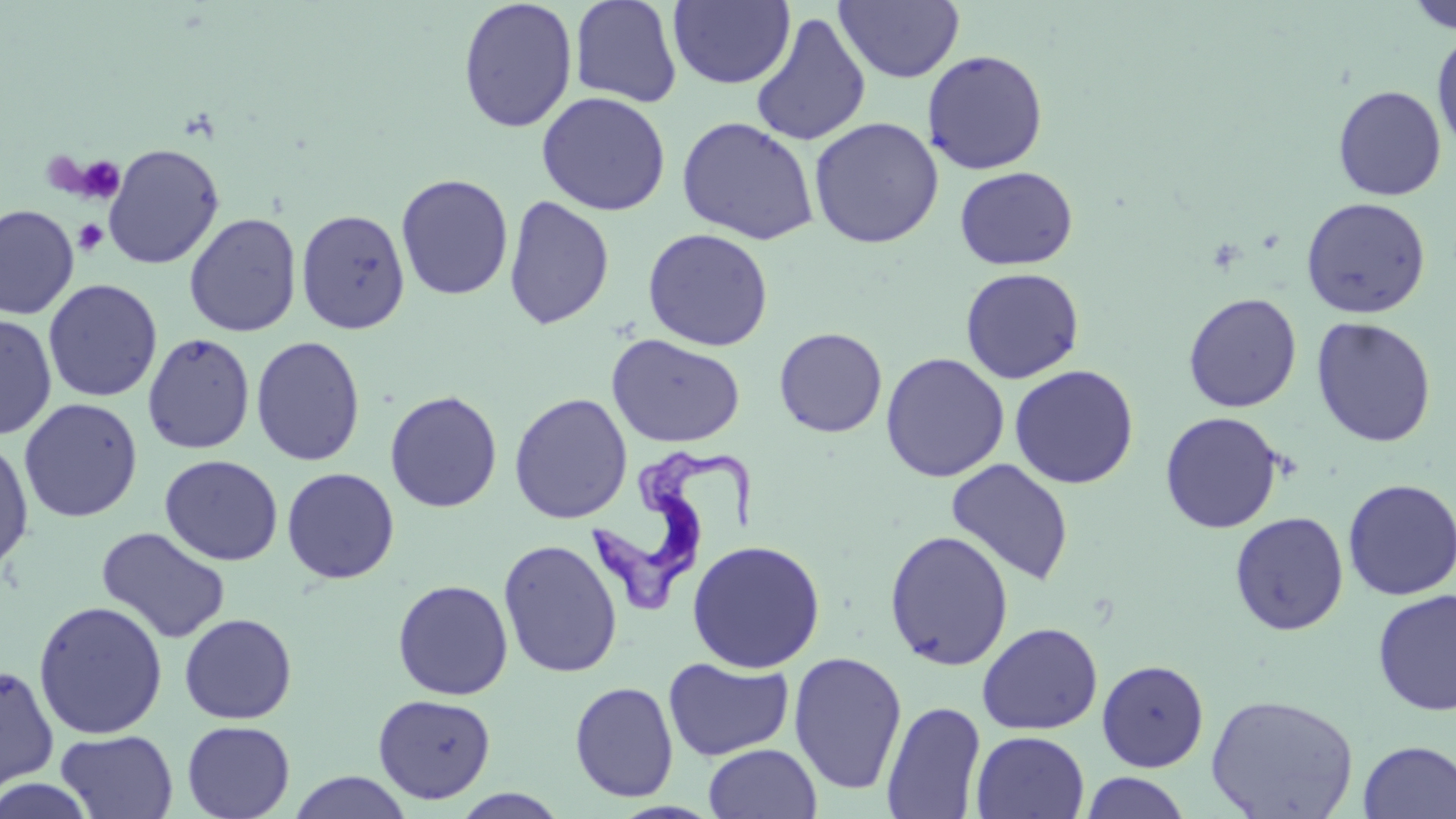

Approximate bounding boxes as (x1, y1, x2, y2) in pixels. Trypanosoma brucei locations: (582, 449, 760, 616). Uninfected red blood cell locations: (457, 0, 578, 133), (569, 0, 683, 109), (669, 0, 795, 89), (835, 1, 965, 84), (1406, 2, 1456, 34), (751, 12, 872, 147), (1432, 30, 1456, 158), (921, 49, 1048, 175), (1332, 85, 1447, 201), (536, 91, 670, 216), (676, 116, 820, 245), (808, 117, 944, 249), (102, 143, 225, 270), (954, 166, 1078, 270), (395, 173, 514, 301), (503, 194, 615, 330), (1300, 197, 1431, 319), (0, 204, 79, 319), (295, 208, 410, 334), (184, 212, 302, 338), (642, 228, 773, 351), (960, 267, 1084, 384), (43, 278, 163, 402), (1182, 292, 1302, 413), (0, 314, 58, 440), (1311, 317, 1436, 448), (774, 327, 887, 437), (142, 332, 255, 454), (606, 334, 745, 448), (251, 336, 365, 467), (880, 352, 1009, 482), (1008, 364, 1139, 489), (384, 389, 503, 513), (508, 393, 632, 524), (18, 397, 144, 523), (1159, 411, 1285, 534), (0, 438, 35, 574), (160, 454, 283, 566), (945, 458, 1074, 586), (281, 467, 400, 584), (1341, 477, 1456, 601), (1229, 511, 1349, 636), (96, 527, 231, 644), (883, 529, 1015, 671), (498, 539, 622, 678), (687, 539, 826, 673), (392, 579, 514, 701), (1372, 587, 1456, 717), (33, 600, 168, 740), (179, 613, 298, 724), (977, 622, 1102, 735), (788, 650, 907, 795), (663, 656, 794, 761), (1096, 659, 1209, 772), (0, 664, 59, 791), (569, 680, 679, 802), (372, 693, 496, 804), (1205, 693, 1359, 819), (881, 700, 987, 819), (181, 720, 295, 819), (56, 730, 178, 817), (970, 731, 1090, 818), (1358, 740, 1456, 819), (703, 743, 822, 818), (287, 771, 413, 819), (1079, 772, 1192, 818), (0, 776, 97, 819), (450, 788, 570, 818). Platelet locations: (76, 155, 125, 204), (73, 219, 109, 255). Slide-level diagnosis: Trypanosoma brucei. Light microscopy. May-Grünwald-Giemsa stain. Thin blood smear. Captured at 1000x magnification. Single field of view. Image is 1456×819 pixels.